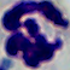

identification = white blood cell
magnification = 1000x
modality = micrograph